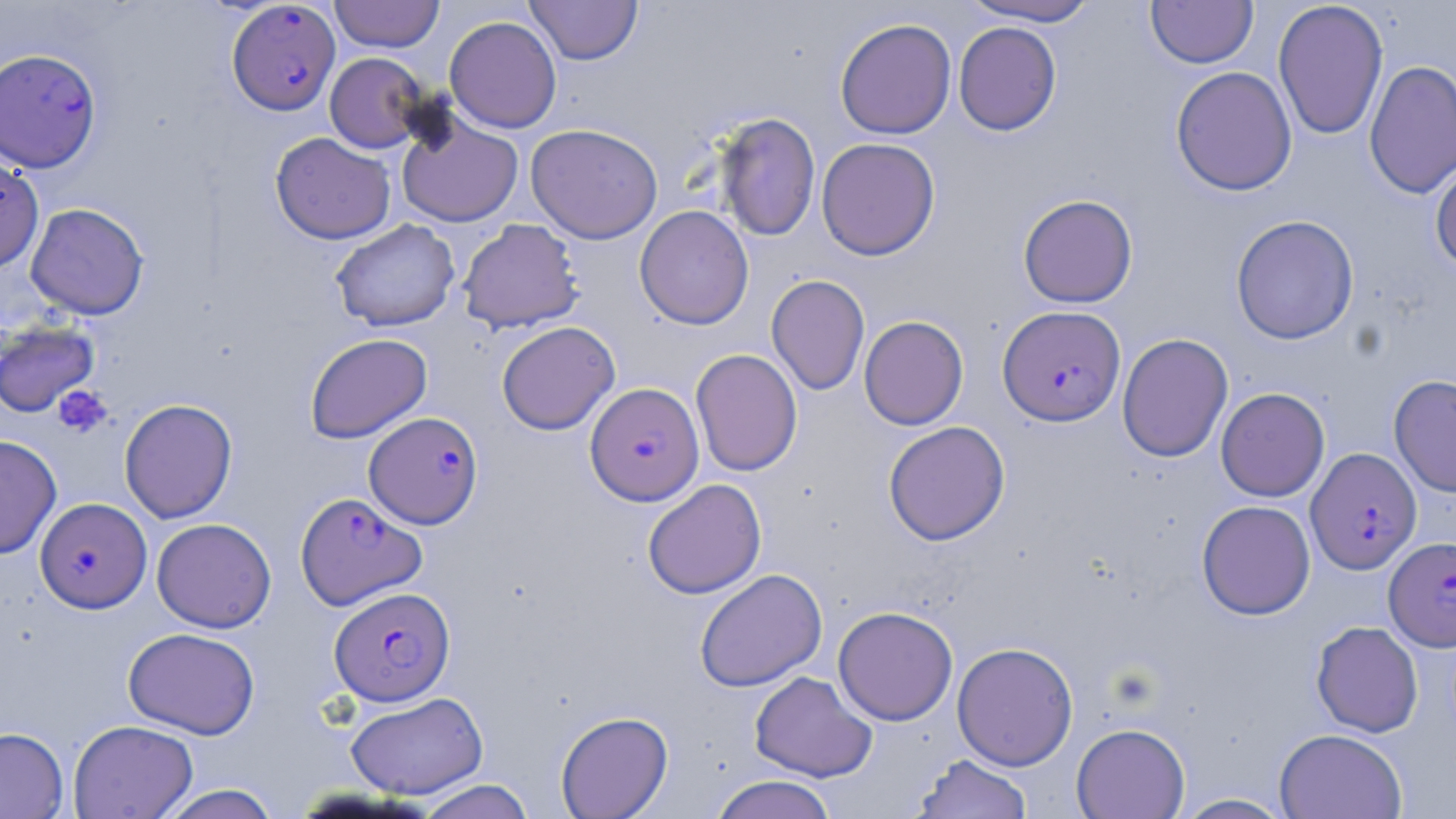

Summary:
  - Coordinate format: approximate bounding boxes as [x1, y1, x2, y2] in pixels
  - Platelet locations: [52, 385, 113, 439]
  - Uninfected red blood cell locations: [329, 0, 445, 52], [525, 0, 643, 65], [959, 0, 1102, 26], [1145, 0, 1258, 69], [1272, 0, 1389, 141], [444, 16, 562, 133], [834, 17, 956, 139], [953, 22, 1061, 136], [325, 52, 428, 153], [1364, 60, 1456, 199], [1170, 66, 1297, 196], [395, 110, 524, 228], [714, 112, 821, 242], [525, 123, 663, 244], [270, 131, 396, 244], [816, 137, 941, 260], [0, 154, 44, 274], [1430, 155, 1456, 273], [1018, 194, 1138, 308], [25, 202, 149, 320], [634, 205, 755, 329], [1230, 215, 1359, 345], [457, 218, 584, 334], [330, 219, 460, 332], [766, 275, 870, 395], [858, 315, 969, 430], [0, 319, 100, 418], [496, 321, 620, 435], [304, 332, 432, 444], [1117, 333, 1233, 463], [690, 348, 802, 476], [1389, 374, 1456, 498], [1215, 387, 1330, 502], [119, 398, 238, 523], [883, 420, 1010, 545], [0, 435, 62, 559], [642, 479, 767, 599], [1196, 500, 1315, 620], [151, 518, 276, 633], [694, 569, 828, 692], [833, 606, 958, 725], [1311, 620, 1423, 737], [123, 627, 260, 738], [952, 641, 1078, 770], [749, 670, 878, 782], [344, 691, 489, 799], [555, 710, 674, 819], [68, 719, 198, 818], [1071, 723, 1190, 818], [0, 726, 68, 819], [1275, 728, 1408, 818], [911, 753, 1032, 819], [710, 774, 838, 819], [415, 779, 536, 819], [156, 783, 282, 819], [1172, 793, 1295, 818]
  - Plasmodium falciparum-infected red blood cell locations: [227, 1, 340, 115], [0, 49, 99, 175], [998, 305, 1126, 426], [586, 382, 703, 505], [363, 411, 484, 529], [1306, 447, 1421, 574], [295, 491, 426, 609], [35, 497, 152, 613], [1384, 536, 1456, 650], [330, 586, 455, 706]
  - Slide-level diagnosis: Plasmodium falciparum
  - Preparation: thin blood smear
  - Field of view: single
  - Stain: May-Grünwald-Giemsa
  - Image size: 1456×819 pixels
  - Magnification: 1000x
  - Modality: optical microscopy